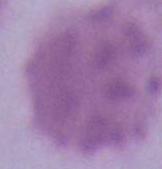

Summary:
  - Magnification: 1000x
  - Modality: photomicrograph
  - Identification: erythrocyte